Locate and identify every blood parasite.
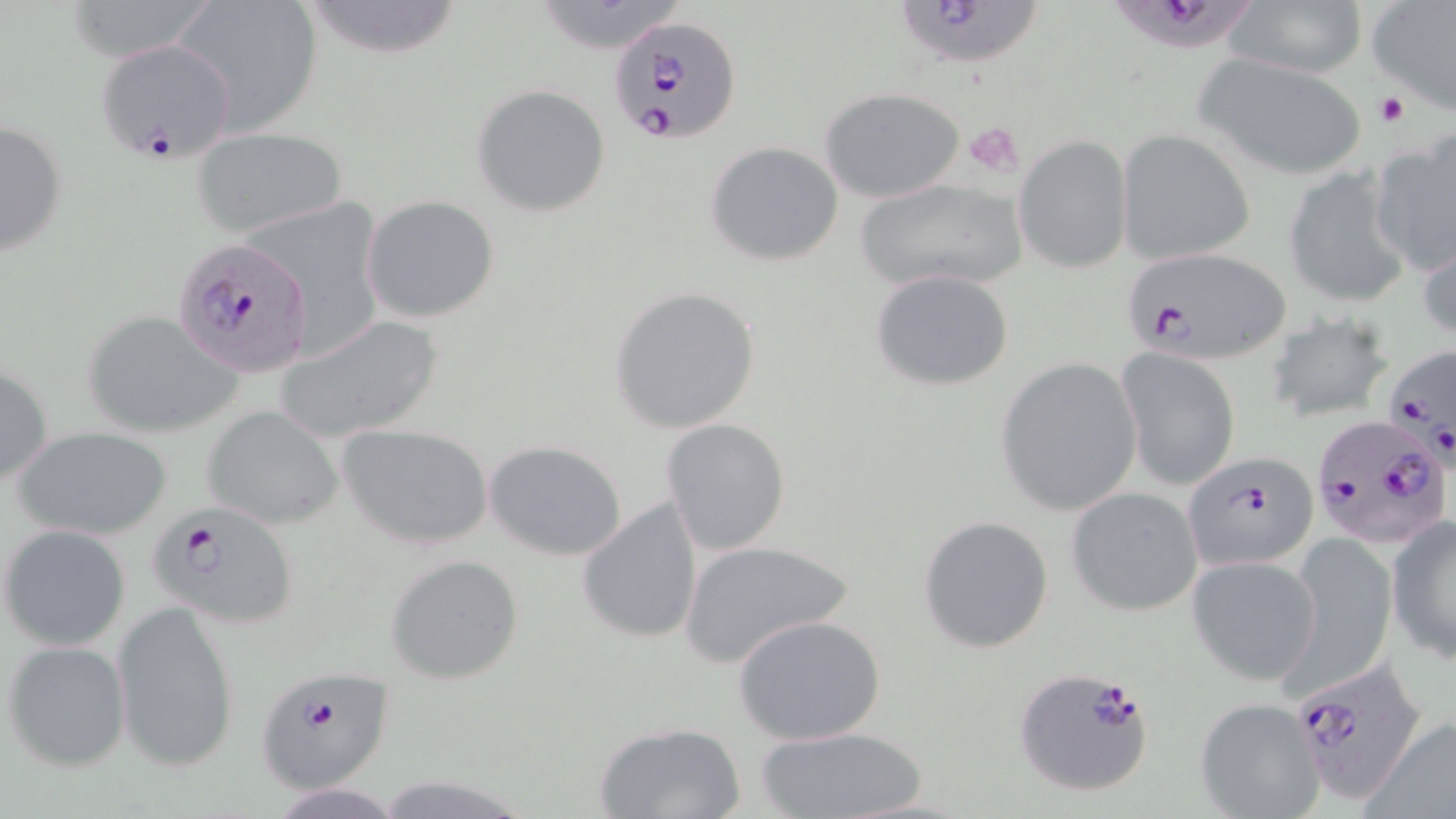
Approximate bounding boxes as (x1,y1)-(x2,y2) corner pairs in pixels.
Plasmodium falciparum-infected red blood cells: (898,1)-(1047,68), (1119,2)-(1267,58), (609,14)-(739,145), (94,37)-(238,161), (172,237)-(315,377), (1123,245)-(1291,365), (1385,344)-(1456,477), (1312,414)-(1455,545), (1183,450)-(1316,572), (150,503)-(300,629), (1285,658)-(1433,804), (252,666)-(397,794), (1013,667)-(1157,797).
No Plasmodium ovale, Plasmodium malariae, Plasmodium vivax, Babesia divergens, or Trypanosoma brucei observed.

Uninfected red blood cell locations: (174,0)-(324,131), (302,0)-(463,59), (529,1)-(689,54), (1366,1)-(1456,113), (1222,2)-(1370,80), (1192,51)-(1371,182), (471,83)-(612,217), (821,88)-(967,203), (1,117)-(70,256), (192,128)-(349,241), (1118,128)-(1255,267), (1371,135)-(1455,278), (1014,136)-(1132,274), (705,140)-(843,267), (1282,166)-(1414,310), (854,176)-(1030,294), (361,195)-(499,322), (1418,223)-(1456,345), (870,269)-(1015,392), (608,285)-(761,434), (79,309)-(241,438), (1262,311)-(1397,426), (276,316)-(445,443), (1116,349)-(1240,491), (995,357)-(1143,517), (0,360)-(52,490), (204,406)-(343,530), (660,419)-(791,557), (339,423)-(493,550), (11,425)-(173,539), (483,439)-(629,562), (1065,486)-(1205,615), (575,497)-(705,647), (1386,514)-(1456,663), (917,515)-(1056,654), (1,523)-(131,649), (1286,535)-(1400,693), (679,538)-(853,669), (386,554)-(526,686), (1187,555)-(1324,687), (112,601)-(240,772), (733,615)-(886,745), (3,640)-(130,775), (1195,697)-(1327,818), (1365,717)-(1456,816), (592,720)-(747,819), (755,726)-(929,819), (375,775)-(533,818), (269,783)-(404,818). Platelet locations: (1377,92)-(1409,126), (963,123)-(1024,176). Slide-level diagnosis: Plasmodium falciparum. Single field of view. Optical microscopy. May-Grünwald-Giemsa-stained preparation. Image is 1456×819 pixels. Captured at 1000x magnification. Thin blood smear.